Give the extent of all uninfected red blood cells.
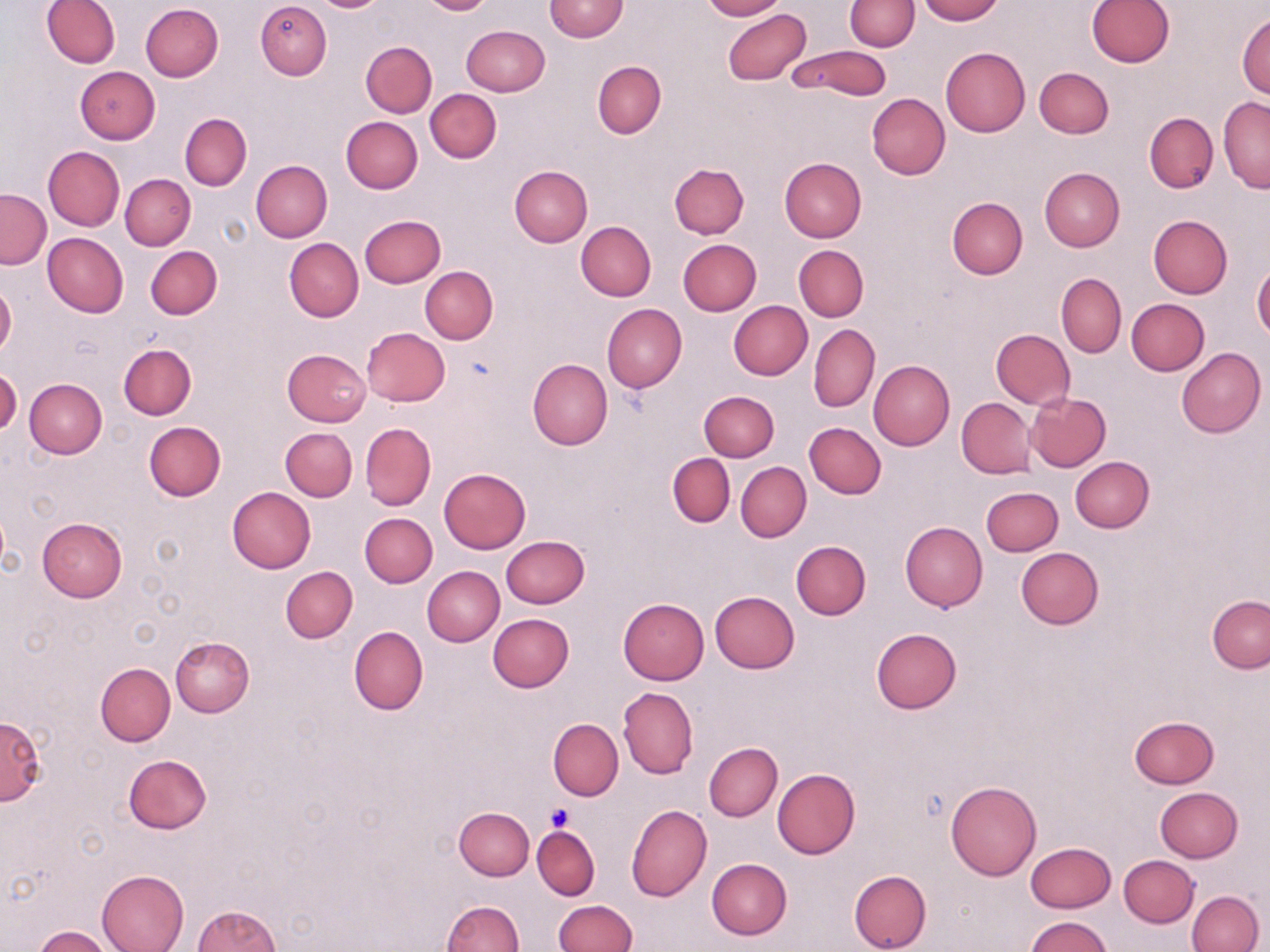
Approximate bounding boxes as named x1/y1/x2/y2 corners in pixels.
Uninfected red blood cells: (x1=42, y1=0, x2=120, y2=68), (x1=256, y1=0, x2=331, y2=80), (x1=314, y1=0, x2=385, y2=11), (x1=418, y1=0, x2=493, y2=15), (x1=544, y1=0, x2=628, y2=41), (x1=699, y1=0, x2=784, y2=20), (x1=915, y1=0, x2=1003, y2=24), (x1=1085, y1=0, x2=1174, y2=68), (x1=845, y1=1, x2=919, y2=51), (x1=140, y1=3, x2=224, y2=82), (x1=722, y1=7, x2=812, y2=86), (x1=1237, y1=15, x2=1270, y2=99), (x1=460, y1=26, x2=549, y2=96), (x1=362, y1=40, x2=437, y2=118), (x1=786, y1=45, x2=892, y2=101), (x1=941, y1=47, x2=1031, y2=136), (x1=592, y1=60, x2=666, y2=139), (x1=74, y1=66, x2=160, y2=144), (x1=1034, y1=67, x2=1114, y2=138), (x1=426, y1=88, x2=502, y2=162), (x1=867, y1=94, x2=950, y2=179), (x1=1218, y1=97, x2=1270, y2=193), (x1=180, y1=113, x2=252, y2=191), (x1=1144, y1=113, x2=1218, y2=193), (x1=341, y1=117, x2=423, y2=193), (x1=43, y1=146, x2=124, y2=230), (x1=778, y1=158, x2=866, y2=242), (x1=250, y1=160, x2=332, y2=242), (x1=670, y1=163, x2=750, y2=238), (x1=510, y1=165, x2=592, y2=248), (x1=1039, y1=168, x2=1123, y2=251), (x1=121, y1=174, x2=195, y2=250), (x1=1, y1=188, x2=50, y2=268), (x1=947, y1=197, x2=1028, y2=279), (x1=360, y1=215, x2=446, y2=287), (x1=1148, y1=215, x2=1232, y2=298), (x1=575, y1=221, x2=655, y2=301), (x1=42, y1=232, x2=128, y2=318), (x1=284, y1=238, x2=364, y2=322), (x1=678, y1=239, x2=761, y2=315), (x1=146, y1=245, x2=222, y2=319), (x1=794, y1=245, x2=868, y2=321), (x1=1252, y1=264, x2=1270, y2=341), (x1=419, y1=267, x2=497, y2=344), (x1=1056, y1=274, x2=1126, y2=357), (x1=0, y1=282, x2=16, y2=357), (x1=1126, y1=298, x2=1210, y2=375), (x1=728, y1=300, x2=813, y2=380), (x1=603, y1=303, x2=686, y2=392), (x1=809, y1=324, x2=880, y2=413), (x1=361, y1=327, x2=451, y2=406), (x1=991, y1=329, x2=1075, y2=409), (x1=118, y1=344, x2=195, y2=420), (x1=1176, y1=347, x2=1265, y2=438), (x1=282, y1=349, x2=371, y2=426), (x1=527, y1=359, x2=613, y2=450), (x1=868, y1=360, x2=955, y2=450), (x1=0, y1=367, x2=21, y2=435), (x1=25, y1=378, x2=107, y2=459), (x1=699, y1=390, x2=779, y2=461), (x1=1025, y1=391, x2=1110, y2=472), (x1=957, y1=398, x2=1035, y2=479), (x1=144, y1=422, x2=226, y2=502), (x1=361, y1=422, x2=436, y2=510), (x1=804, y1=422, x2=886, y2=498), (x1=280, y1=428, x2=357, y2=500), (x1=667, y1=453, x2=735, y2=528), (x1=1070, y1=458, x2=1154, y2=532), (x1=736, y1=462, x2=810, y2=542), (x1=439, y1=468, x2=531, y2=552), (x1=981, y1=486, x2=1062, y2=556), (x1=226, y1=487, x2=316, y2=573), (x1=360, y1=513, x2=437, y2=587), (x1=37, y1=518, x2=126, y2=602), (x1=899, y1=522, x2=988, y2=612), (x1=500, y1=535, x2=589, y2=609), (x1=791, y1=541, x2=870, y2=619), (x1=1016, y1=548, x2=1104, y2=630), (x1=280, y1=565, x2=357, y2=643), (x1=423, y1=566, x2=504, y2=646), (x1=710, y1=590, x2=799, y2=673), (x1=1207, y1=596, x2=1269, y2=672), (x1=618, y1=598, x2=709, y2=685), (x1=488, y1=613, x2=574, y2=691), (x1=349, y1=626, x2=428, y2=715), (x1=871, y1=628, x2=962, y2=714), (x1=169, y1=636, x2=254, y2=717), (x1=96, y1=662, x2=175, y2=745), (x1=618, y1=687, x2=698, y2=779), (x1=551, y1=702, x2=696, y2=786), (x1=0, y1=715, x2=46, y2=805), (x1=1128, y1=716, x2=1220, y2=789), (x1=548, y1=718, x2=623, y2=801), (x1=703, y1=743, x2=782, y2=821), (x1=124, y1=754, x2=212, y2=835), (x1=771, y1=768, x2=859, y2=859), (x1=946, y1=780, x2=1041, y2=879), (x1=1154, y1=787, x2=1242, y2=862), (x1=626, y1=804, x2=712, y2=901), (x1=454, y1=807, x2=534, y2=880), (x1=532, y1=825, x2=600, y2=900), (x1=1025, y1=842, x2=1116, y2=912), (x1=1119, y1=854, x2=1198, y2=927), (x1=707, y1=858, x2=792, y2=940), (x1=97, y1=869, x2=189, y2=952), (x1=849, y1=869, x2=932, y2=952), (x1=1187, y1=890, x2=1264, y2=952), (x1=441, y1=900, x2=524, y2=952), (x1=552, y1=900, x2=637, y2=952), (x1=191, y1=904, x2=280, y2=952), (x1=1025, y1=917, x2=1112, y2=952), (x1=33, y1=925, x2=112, y2=952).

Platelet locations: (x1=545, y1=804, x2=574, y2=832). Slide-level diagnosis: negative for blood parasites. May-Grünwald-Giemsa-stained preparation. Thin blood film. One field of a larger specimen. 1000x magnification. Image is 1270×952 pixels. Optical microscopy.